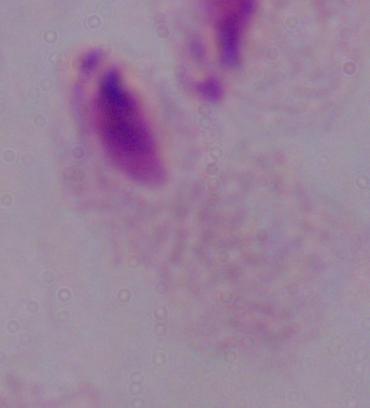
identification = trichomonad
magnification = 1000x
modality = micrograph